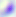
identification = Toxoplasma gondii
modality = micrograph
magnification = 400x